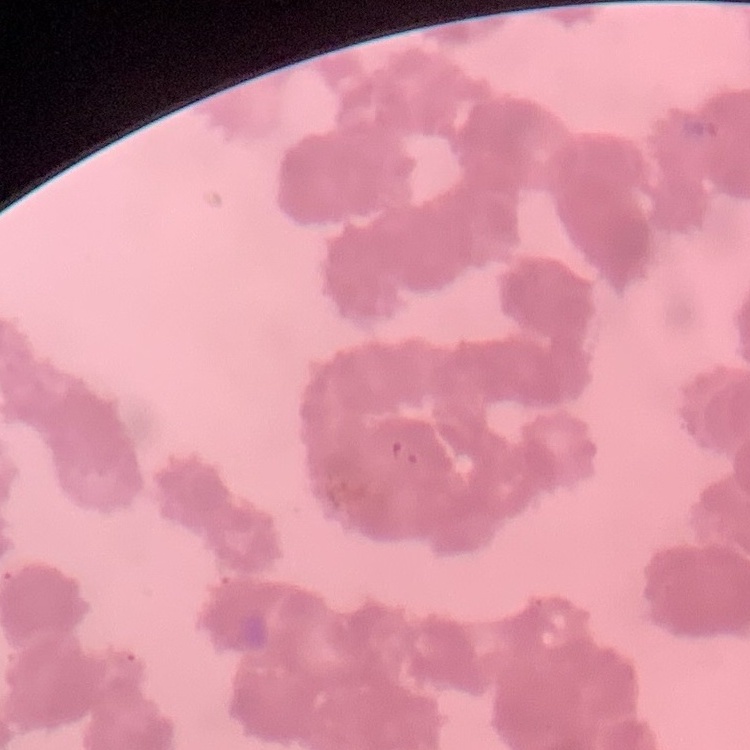
{
  "erythrocyte_morphology": "rouleaux formation",
  "image_type": "square crop of a larger photomicrograph",
  "stain": "Field's or Giemsa",
  "preparation": "thin blood smear"
}